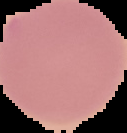

preparation = thin blood smear
malaria status = uninfected
image size = 127×133 pixels
image type = segmented cell region on a black background